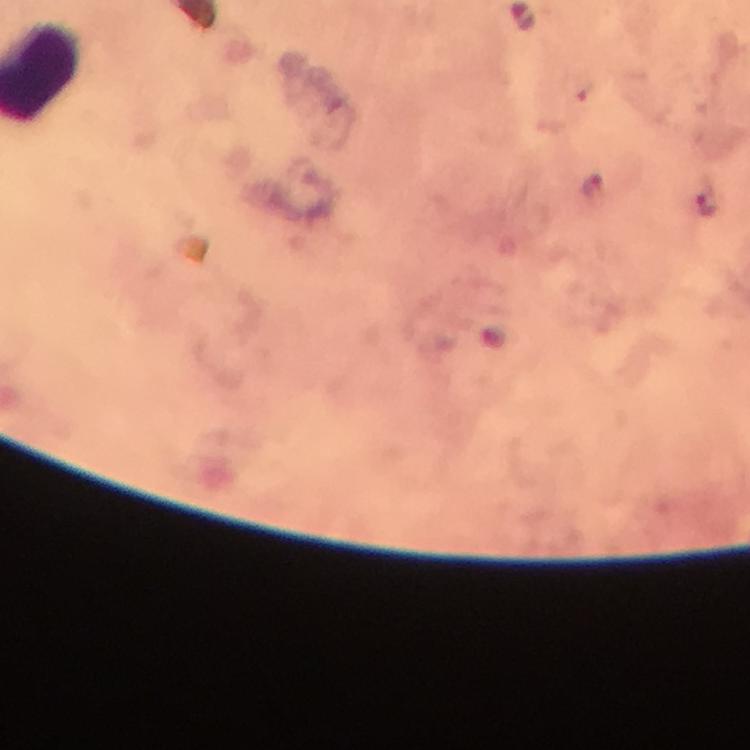 Approximate centers as {x, y} in pixels. Malaria parasite locations: {594, 185}, {705, 205}. Giemsa stain. Photographed with a smartphone mounted on the microscope. Thick blood smear. 100x magnification. A crop from one field of view. Immersion oil applied. Image is 750×750 pixels. From a diagnostic examination for malaria.